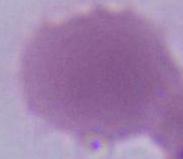

Summary:
  - Identification: erythrocyte
  - Modality: micrograph
  - Magnification: 1000x